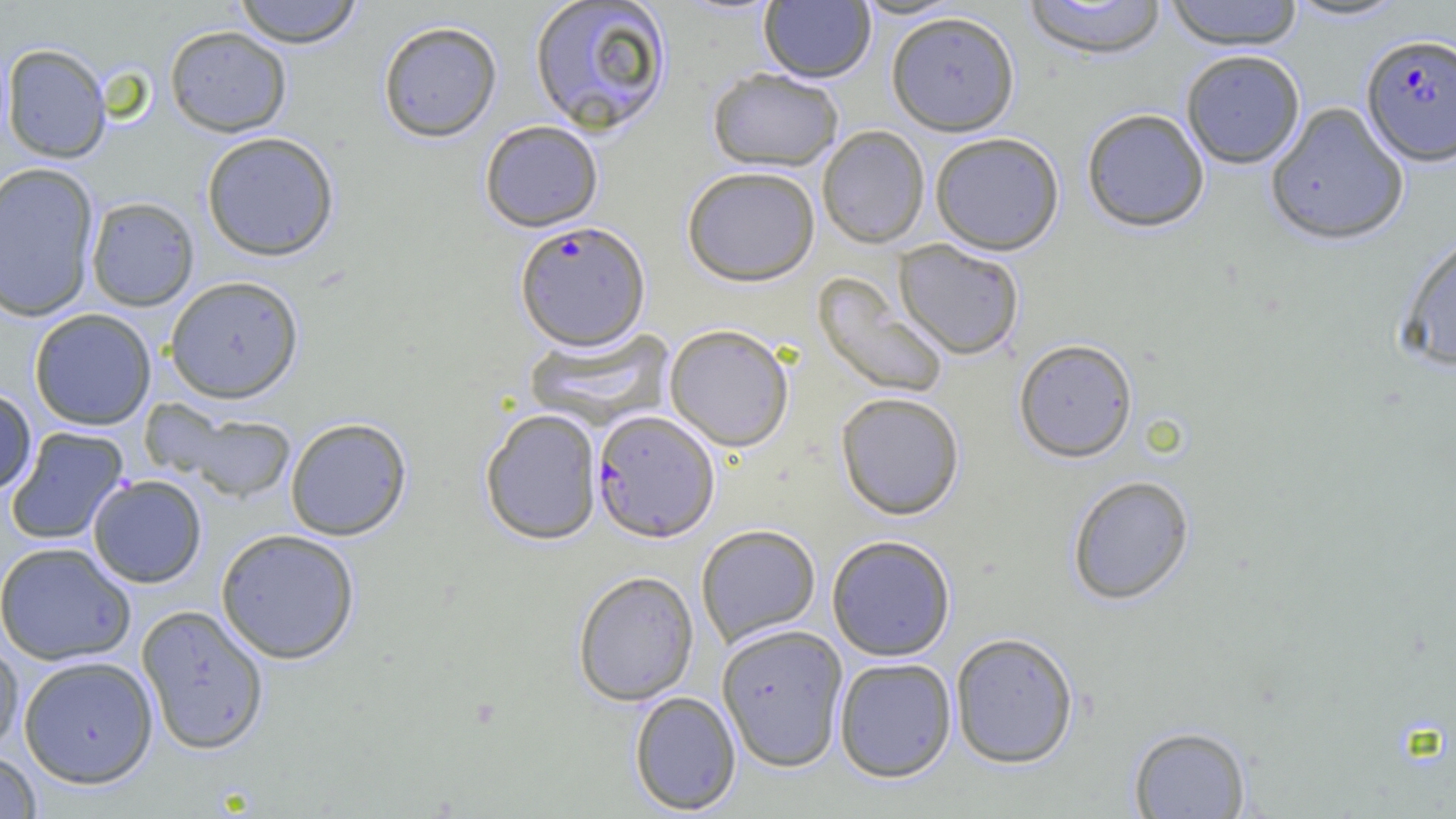
Approximate bounding boxes as [x1, y1, x2, y2] in pixels. Uninfected red blood cell locations: [233, 0, 364, 48], [528, 0, 673, 136], [853, 0, 964, 20], [1164, 0, 1304, 52], [1284, 0, 1411, 23], [759, 1, 876, 84], [1022, 1, 1167, 62], [886, 13, 1020, 137], [377, 20, 503, 143], [164, 25, 292, 137], [1, 43, 112, 163], [1181, 52, 1305, 169], [707, 69, 843, 173], [1266, 103, 1409, 247], [1081, 109, 1210, 235], [480, 120, 604, 232], [817, 126, 930, 249], [201, 131, 339, 261], [930, 133, 1065, 255], [0, 162, 101, 322], [682, 167, 820, 287], [86, 196, 200, 311], [1396, 228, 1456, 373], [893, 242, 1025, 361], [812, 275, 949, 399], [165, 276, 304, 403], [28, 308, 157, 431], [664, 324, 794, 453], [524, 327, 675, 430], [1014, 339, 1138, 464], [0, 387, 37, 495], [836, 392, 965, 521], [153, 402, 297, 502], [480, 408, 603, 545], [284, 417, 412, 541], [6, 427, 129, 546], [88, 475, 207, 588], [1067, 475, 1195, 606], [695, 524, 821, 649], [215, 529, 360, 664], [827, 535, 956, 662], [0, 542, 136, 666], [572, 571, 699, 706], [136, 604, 271, 755], [716, 624, 849, 773], [950, 632, 1079, 769], [0, 635, 24, 755], [18, 656, 159, 789], [834, 657, 957, 783], [629, 691, 742, 815], [1128, 725, 1251, 818], [0, 750, 42, 818]. Plasmodium falciparum-infected red blood cell locations: [1361, 35, 1456, 168], [514, 221, 650, 351], [592, 410, 720, 543]. Slide-level diagnosis: Plasmodium falciparum. Captured at 1000x magnification. Optical microscopy. Image is 1456×819 pixels. Thin blood film. One field of a larger specimen.